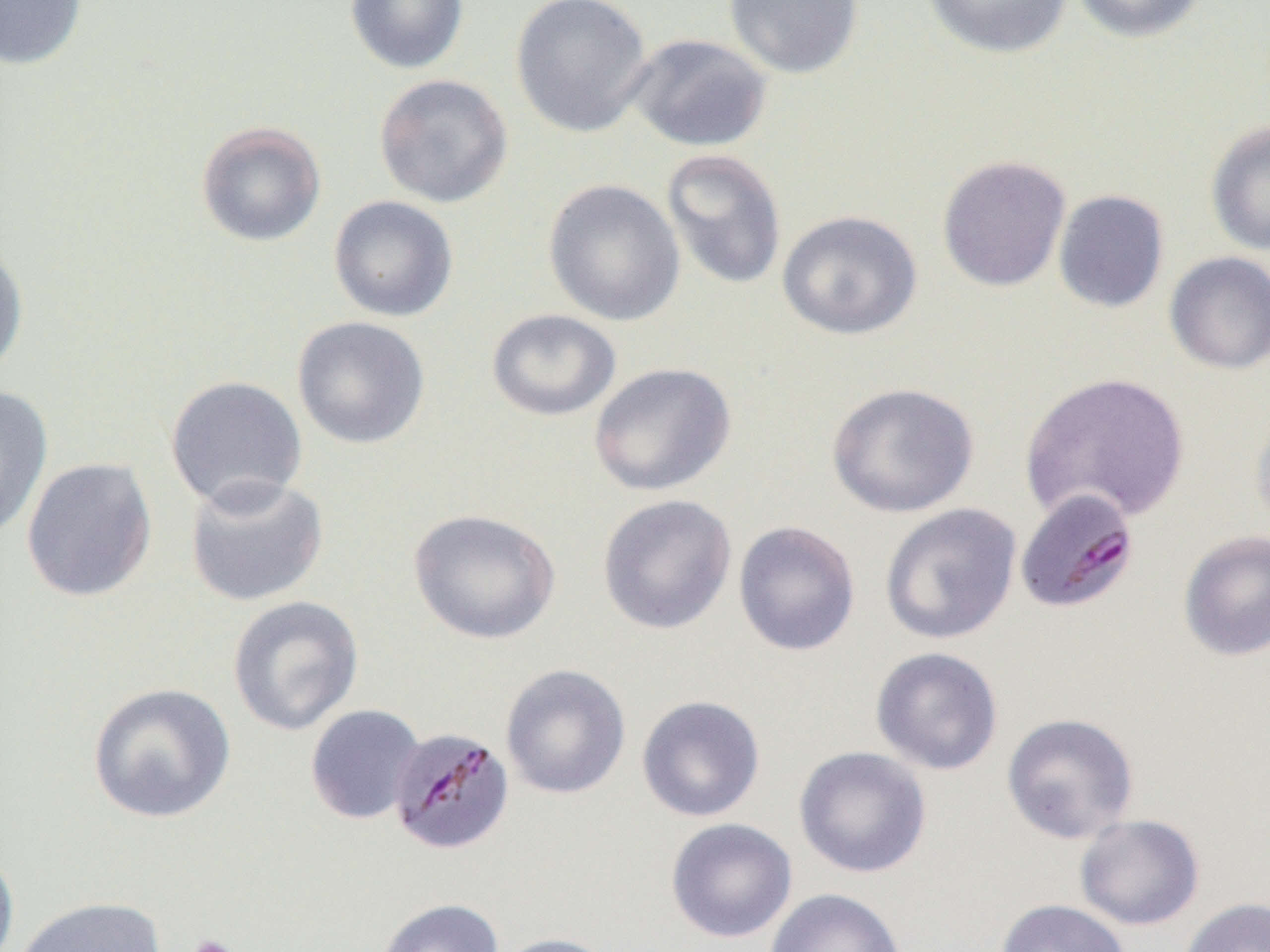 Approximate bounding boxes as (x1,y1)-(x2,y2) corner pairs in pixels. Platelet locations: (187,934)-(240,952). Uninfected red blood cell locations: (0,0)-(87,70), (344,0)-(470,74), (510,0)-(653,138), (723,0)-(864,80), (919,0)-(1075,60), (1071,0)-(1208,44), (625,32)-(773,153), (373,73)-(513,208), (1205,120)-(1270,257), (195,121)-(327,247), (660,148)-(788,292), (936,154)-(1072,292), (542,179)-(686,327), (1052,189)-(1170,313), (328,195)-(459,322), (776,209)-(923,341), (0,238)-(30,382), (1164,251)-(1270,375), (486,309)-(622,422), (292,316)-(431,450), (588,362)-(737,497), (1018,371)-(1191,525), (164,375)-(308,513), (825,381)-(979,518), (0,384)-(54,541), (1250,401)-(1270,537), (21,457)-(158,602), (183,472)-(330,607), (597,494)-(737,635), (879,502)-(1022,645), (408,508)-(561,645), (733,520)-(861,656), (1178,530)-(1270,662), (227,596)-(364,736), (870,646)-(1004,775), (500,663)-(631,800), (87,682)-(236,824), (636,694)-(766,822), (305,704)-(425,825), (1001,712)-(1139,844), (793,746)-(932,879), (1074,814)-(1204,931), (665,818)-(798,944), (0,843)-(20,952), (764,888)-(908,952), (11,896)-(167,952), (1177,896)-(1270,952), (375,898)-(504,952), (995,898)-(1132,952), (491,932)-(620,952). Plasmodium malariae-infected red blood cell locations: (1014,487)-(1139,613), (388,725)-(515,855). Slide-level diagnosis: Plasmodium malariae. Thin blood film. Captured at 1000x magnification. Image is 1270×952 pixels. Optical microscopy. One field of a larger specimen.